Name the cell type shown.
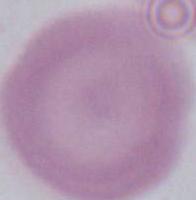

This is an erythrocyte.

magnification = 1000x
modality = micrograph